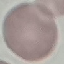
{
  "result": "negative for malaria parasites",
  "preparation": "thin blood film",
  "stain": "Giemsa",
  "image_type": "automatically extracted cell patch, resized to 64 × 64 pixels",
  "capture": "smartphone camera at the microscope eyepiece"
}